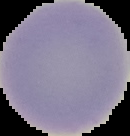

Summary:
  - Image size: 130×136 pixels
  - Preparation: thin blood film
  - Result: negative for malaria parasites
  - Image type: cell region segmented out of the field of view; surrounding area masked to black